Name the parasite shown.
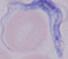

This is a trypanosome.

modality = micrograph
magnification = 1000x